Identify the preparation type.
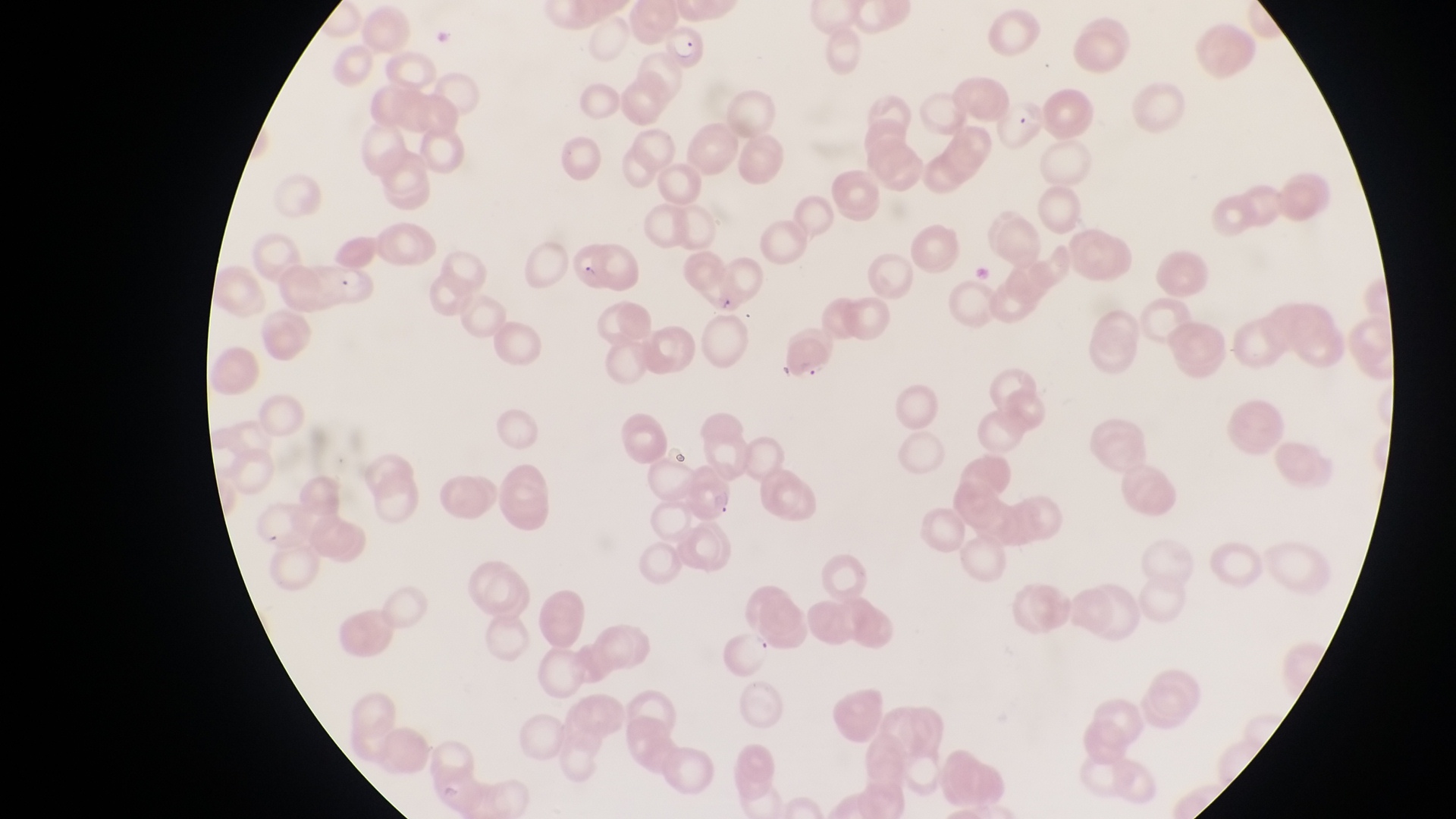

This is a thin smear.

parasitised red blood cell locations = approximate bounding boxes as (left, top, right, bottom) in pixels: (658, 10, 708, 73), (993, 98, 1045, 147)
country = Uganda
field of view = single
artifact (platelet-like body, stain precipitate, or debris) locations = approximate bounding boxes as (left, top, right, bottom) in pixels: (435, 24, 458, 50)
capture = smartphone photograph through the eyepiece of an Olympus CX-23 microscope
magnification = 1000x
image size = 1456×819 pixels